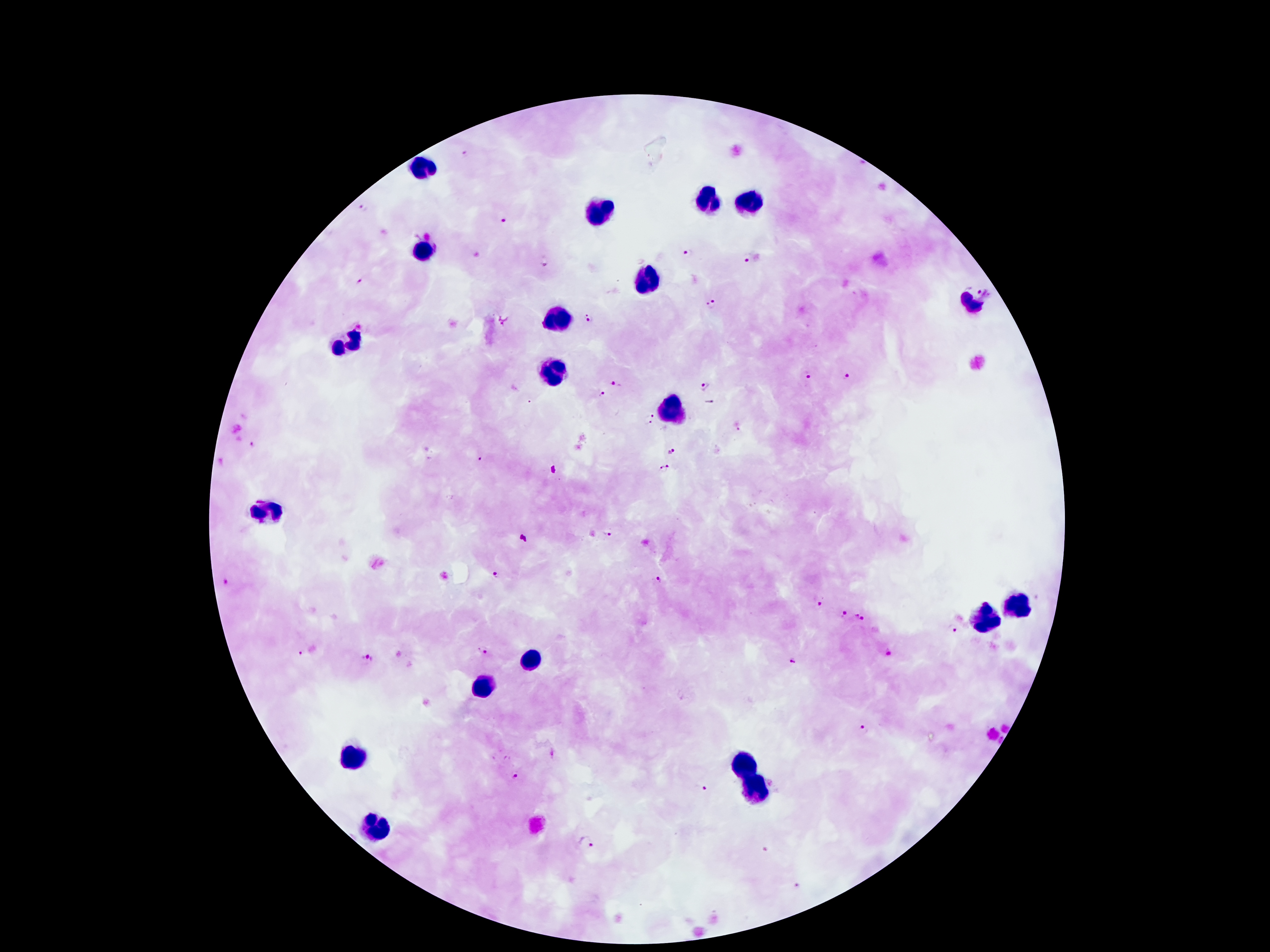

Approximate object centers, in pixels from the top-left corner. Leukocyte locations: (x=421, y=168), (x=706, y=197), (x=755, y=199), (x=599, y=209), (x=425, y=252), (x=646, y=283), (x=972, y=303), (x=562, y=315), (x=343, y=344), (x=554, y=377), (x=675, y=410), (x=267, y=510), (x=1017, y=606), (x=989, y=619), (x=534, y=658), (x=482, y=688), (x=351, y=760), (x=745, y=764), (x=759, y=791), (x=376, y=828). Malaria parasite locations: (x=466, y=152), (x=362, y=206), (x=504, y=220), (x=687, y=253), (x=748, y=259), (x=545, y=261), (x=361, y=279), (x=980, y=290), (x=712, y=305), (x=589, y=317), (x=504, y=319), (x=809, y=376), (x=845, y=377), (x=614, y=383), (x=705, y=385), (x=603, y=393), (x=711, y=404), (x=650, y=419), (x=738, y=427), (x=251, y=444), (x=671, y=451), (x=481, y=461), (x=669, y=465), (x=662, y=470), (x=607, y=534), (x=496, y=573), (x=660, y=581), (x=226, y=582), (x=817, y=604), (x=842, y=614), (x=862, y=616), (x=952, y=629), (x=483, y=650), (x=887, y=650), (x=301, y=653), (x=367, y=660), (x=793, y=661), (x=862, y=728), (x=514, y=775), (x=703, y=787), (x=587, y=842). Patient malaria status: positive for Plasmodium falciparum. Single field of view. Giemsa-stained preparation. Thick peripheral-blood smear. 100x magnification. Image is 1270×952 pixels. Photographed through the microscope eyepiece with a smartphone camera.